Assess this cell for malaria.
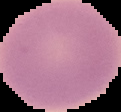

Uninfected.

Summary:
  - Image size: 121×112 pixels
  - Image type: cell region segmented out of the field of view; surrounding area masked to black
  - Preparation: thin blood smear